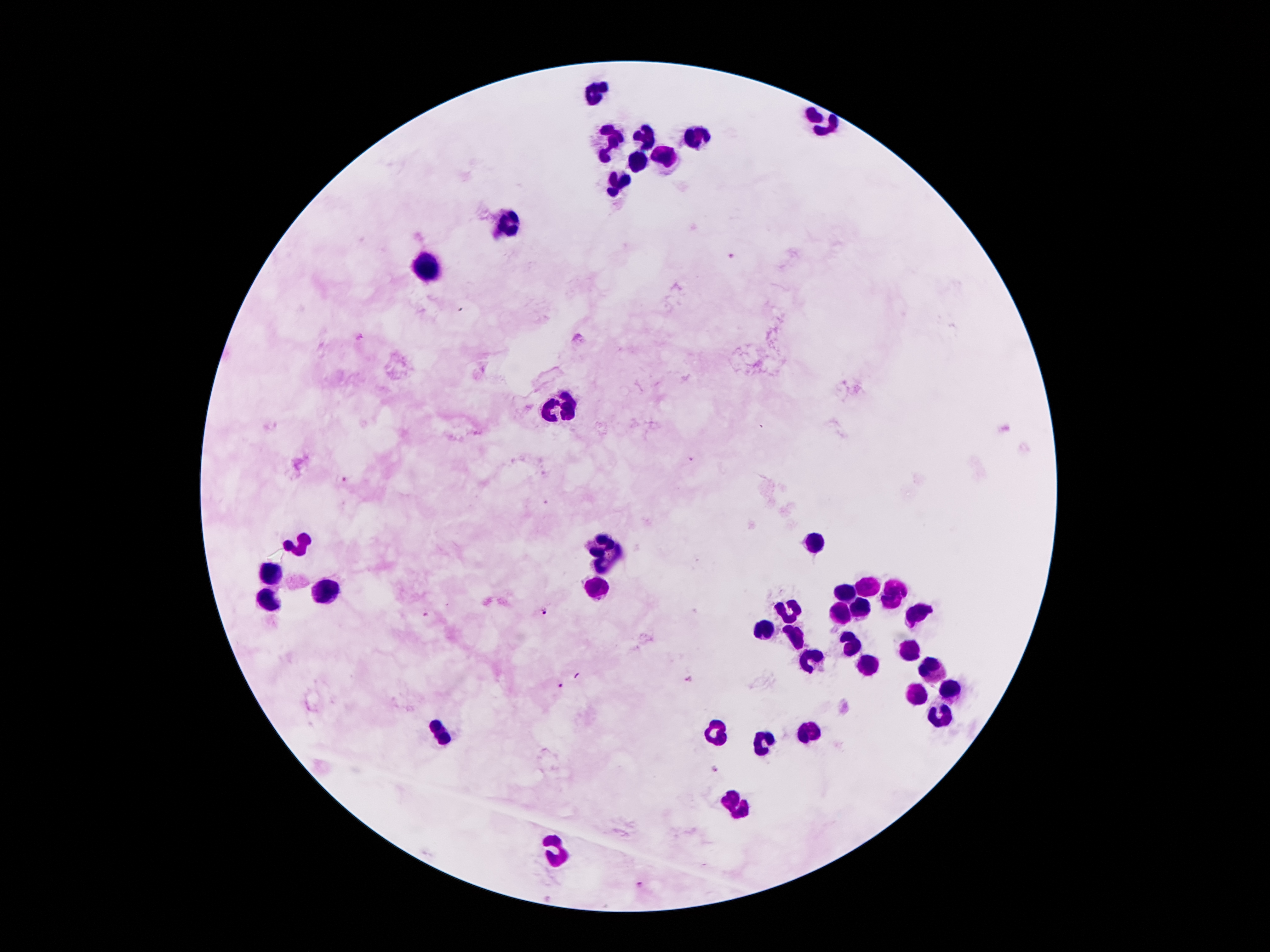
Approximate centers as (x, y) in pixels. Leukocyte locations: (594, 88), (825, 124), (642, 132), (697, 138), (610, 142), (665, 159), (642, 161), (621, 184), (508, 225), (430, 268), (566, 407), (600, 542), (304, 544), (818, 544), (618, 549), (604, 567), (277, 570), (867, 586), (329, 588), (892, 588), (602, 590), (844, 591), (268, 603), (858, 606), (789, 612), (841, 612), (917, 612), (768, 629), (797, 633), (852, 643), (911, 647), (808, 663), (869, 665), (930, 666), (917, 691), (951, 691), (940, 717), (715, 734), (812, 734), (440, 735), (768, 746), (739, 803), (558, 851). Malaria parasite locations: (731, 257), (362, 338), (691, 460), (345, 479), (545, 501), (545, 612), (428, 616), (688, 679), (559, 686), (716, 769), (640, 884). 100x magnification. One field from this slide. Smartphone photograph taken through the microscope eyepiece. Image is 1270×952 pixels. Giemsa-stained preparation. Patient malaria status: positive for Plasmodium falciparum. Thick blood film.